Describe the morphology of the erythrocytes.
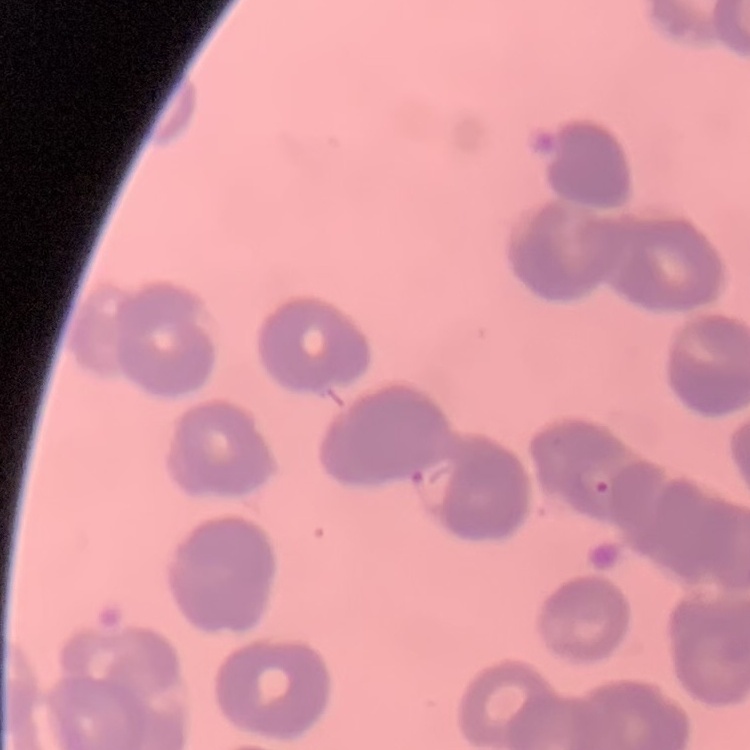

They show rouleaux formation.

Summary:
  - Stain: Field's or Giemsa
  - Image type: square crop of a larger photomicrograph
  - Preparation: thin blood film